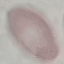

Result: no malaria parasites detected. Cell patch, automatically extracted from a larger field of view and resized to 64 × 64 pixels. Giemsa stain. Thin blood film. Acquired by smartphone through the microscope eyepiece.